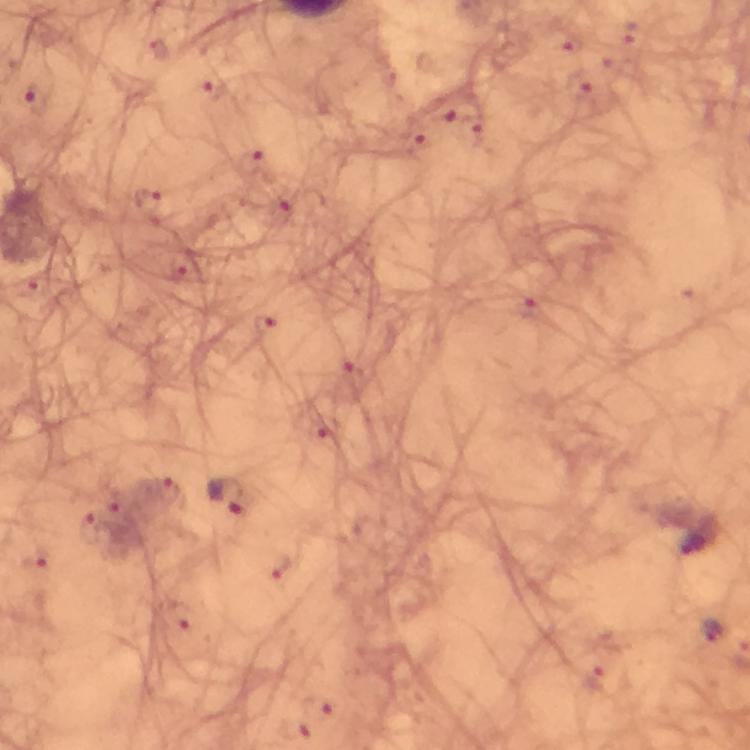

Approximate centers as (x, y) in pixels.
Summary:
  - Plasmodium parasite locations: (567, 40), (579, 85), (212, 93), (34, 102), (446, 110), (414, 139), (250, 163), (146, 201), (280, 208), (526, 306), (264, 325), (228, 497), (693, 541), (710, 629)
  - Preparation: thick smear
  - Magnification: 100x
  - Immersion oil: used
  - Cropped from: a single field of view
  - Capture: smartphone camera through the microscope
  - Stain: Giemsa
  - Context: from a malaria diagnostic workup
  - Image size: 750×750 pixels